Locate every Plasmodium falciparum-infected red blood cell.
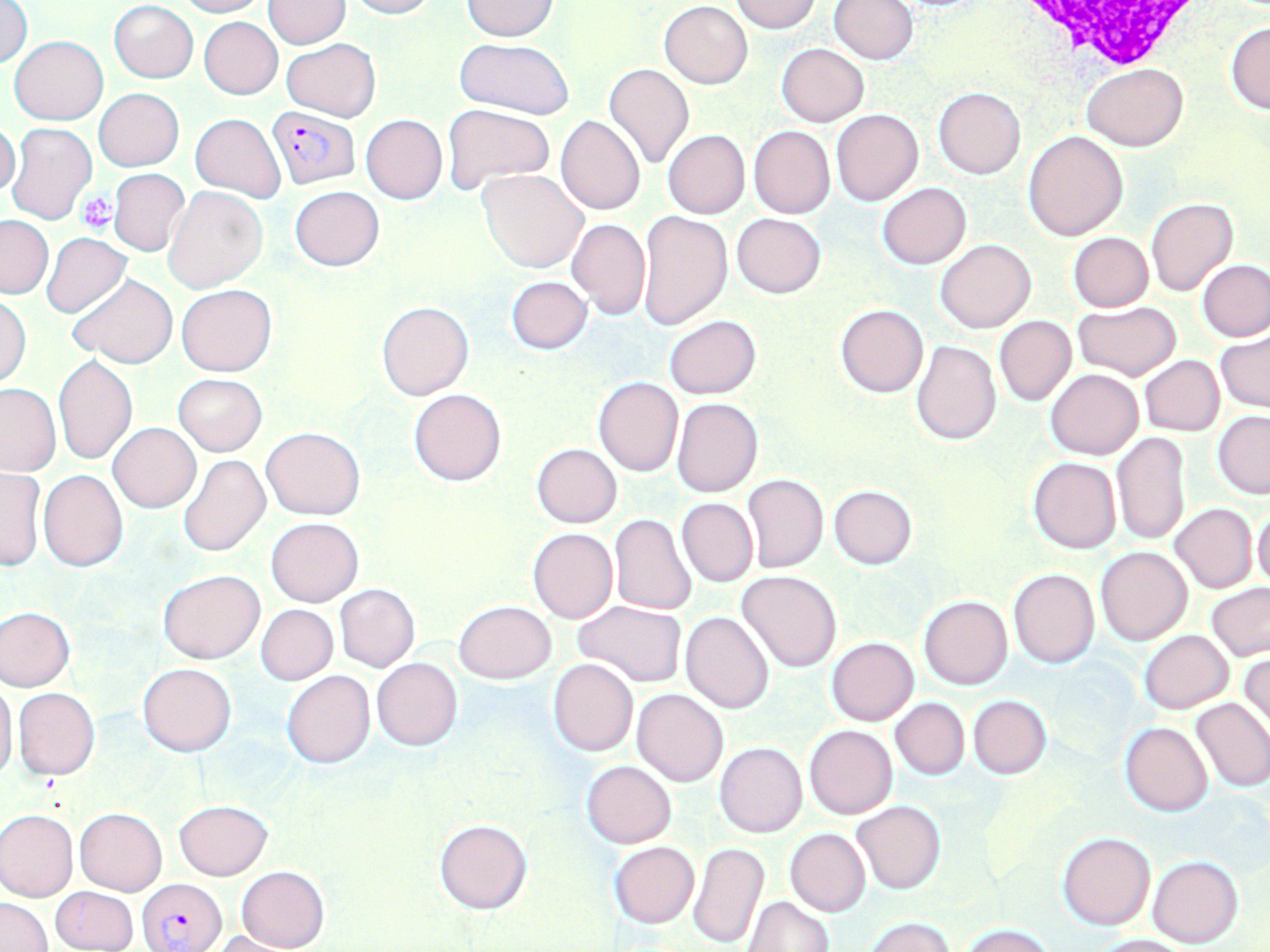

Approximate bounding boxes as (x1, y1, x2, y2) in pixels.
Plasmodium falciparum-infected red blood cells: (267, 106, 360, 190), (138, 877, 227, 952).

Summary:
  - Platelet locations: (78, 190, 119, 234)
  - Uninfected red blood cell locations: (173, 0, 267, 17), (341, 0, 436, 19), (730, 0, 821, 33), (829, 0, 918, 64), (0, 1, 32, 69), (109, 1, 198, 82), (264, 1, 349, 48), (461, 1, 558, 41), (659, 1, 752, 88), (199, 17, 282, 99), (1225, 22, 1270, 114), (9, 35, 109, 125), (454, 37, 576, 119), (282, 38, 382, 121), (777, 43, 868, 126), (602, 63, 693, 170), (1082, 63, 1188, 150), (933, 87, 1026, 178), (94, 88, 183, 171), (442, 105, 554, 193), (832, 109, 923, 206), (190, 114, 285, 202), (360, 114, 447, 204), (556, 115, 646, 215), (0, 117, 20, 199), (8, 121, 97, 226), (749, 125, 835, 218), (662, 130, 750, 218), (1022, 130, 1127, 241), (509, 148, 642, 254), (107, 168, 190, 257), (478, 169, 589, 272), (878, 182, 970, 269), (289, 185, 384, 271), (164, 186, 268, 293), (1146, 198, 1239, 297), (637, 211, 732, 330), (731, 213, 825, 297), (0, 217, 53, 299), (567, 218, 651, 320), (41, 232, 132, 318), (1069, 233, 1154, 311), (935, 239, 1034, 332), (1198, 259, 1270, 341), (68, 274, 177, 367), (505, 275, 592, 354), (176, 283, 277, 376), (1, 295, 32, 387), (377, 301, 473, 399), (1074, 302, 1181, 381), (836, 304, 929, 398), (664, 315, 761, 400), (994, 315, 1077, 406), (1216, 330, 1270, 413), (912, 340, 1001, 445), (54, 355, 137, 465), (1139, 355, 1224, 436), (1046, 368, 1143, 459), (173, 374, 267, 456), (593, 377, 684, 477), (0, 383, 60, 476), (409, 388, 506, 486), (672, 397, 763, 496), (1212, 410, 1270, 498), (108, 423, 200, 513), (261, 427, 366, 520), (1112, 432, 1191, 546), (531, 443, 622, 527), (178, 455, 270, 558), (1027, 457, 1122, 553), (1, 467, 44, 572), (38, 469, 128, 571), (741, 474, 829, 574), (828, 484, 917, 568), (677, 498, 757, 587), (1251, 502, 1270, 591), (1170, 503, 1257, 592), (609, 513, 697, 615), (266, 518, 363, 606), (528, 527, 617, 623), (1095, 547, 1193, 646), (157, 567, 265, 664), (1008, 568, 1099, 667), (736, 571, 842, 674), (334, 583, 420, 672), (1206, 584, 1270, 660), (919, 595, 1012, 689), (454, 600, 555, 684), (572, 600, 687, 687), (702, 602, 825, 704), (255, 604, 338, 685), (0, 607, 75, 691), (680, 612, 774, 714), (1139, 629, 1233, 713), (826, 637, 919, 725), (1240, 650, 1269, 739), (371, 657, 462, 750), (547, 658, 638, 757), (138, 662, 236, 755), (282, 669, 375, 768), (0, 679, 18, 784), (13, 689, 99, 779), (632, 689, 728, 786), (968, 695, 1051, 778), (890, 696, 970, 779), (1190, 698, 1270, 792), (1120, 721, 1213, 816), (804, 724, 899, 820), (714, 742, 807, 837), (581, 760, 676, 848), (174, 800, 272, 880), (853, 800, 945, 893), (0, 808, 77, 902), (75, 808, 168, 896), (434, 818, 532, 915), (785, 828, 870, 916), (1057, 832, 1156, 930), (609, 841, 699, 928), (687, 841, 768, 950), (1148, 855, 1243, 948), (235, 865, 330, 952), (51, 887, 136, 951), (745, 896, 832, 951), (1, 897, 51, 952), (865, 918, 956, 952), (961, 923, 1055, 951), (207, 931, 301, 951), (1093, 933, 1189, 952)
  - White blood cell locations: (999, 0, 1206, 69)
  - Slide-level diagnosis: Plasmodium falciparum
  - Preparation: thin blood smear
  - Image size: 1270×952 pixels
  - Stain: May-Grünwald-Giemsa
  - Field of view: single
  - Magnification: 1000x
  - Modality: optical microscopy